Report the malaria status of this cell.
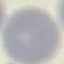

It is uninfected.

Summary:
  - Stain: Giemsa
  - Image type: automatically extracted cell patch, resized to 64 × 64 pixels
  - Capture: smartphone camera at the microscope eyepiece
  - Preparation: thin blood film